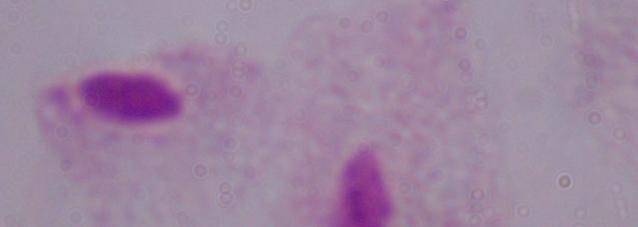
{
  "identification": "trichomonad",
  "modality": "micrograph",
  "magnification": "1000x"
}